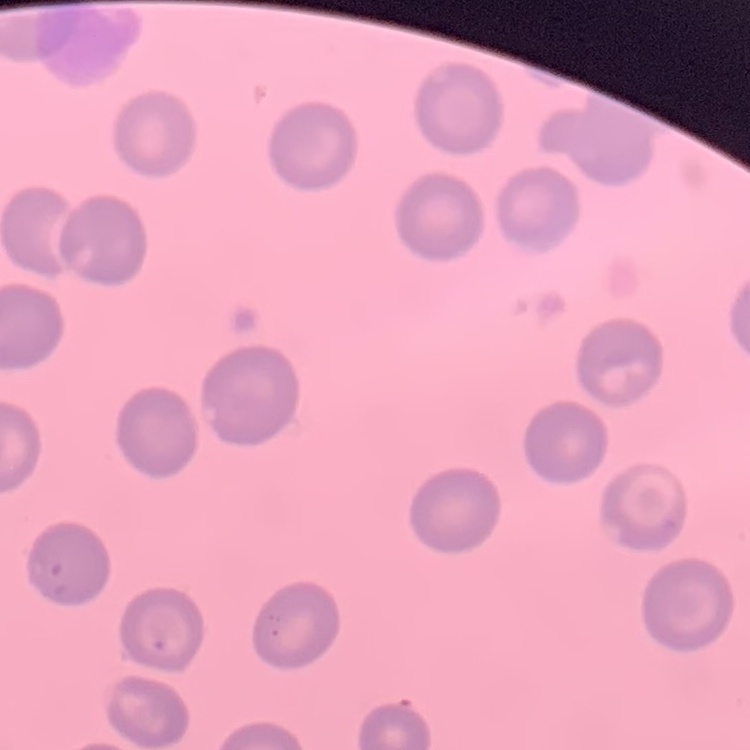

Summary:
  - Red blood cell morphology: no rouleaux formation
  - Stain: Field's or Giemsa
  - Preparation: thin blood smear
  - Image type: one tile cut from a larger photomicrograph